Assess this cell for malaria.
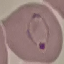

It is parasitized.

image type = cell patch, automatically extracted from a larger field of view and resized to 64 × 64 pixels
capture = smartphone through the microscope eyepiece
stain = Giemsa
preparation = thin blood smear